Assess this cell for malaria.
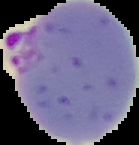

Parasitized.

Summary:
  - Image type: cell region segmented out of the field of view; surrounding area masked to black
  - Image size: 139×145 pixels
  - Preparation: thin blood smear